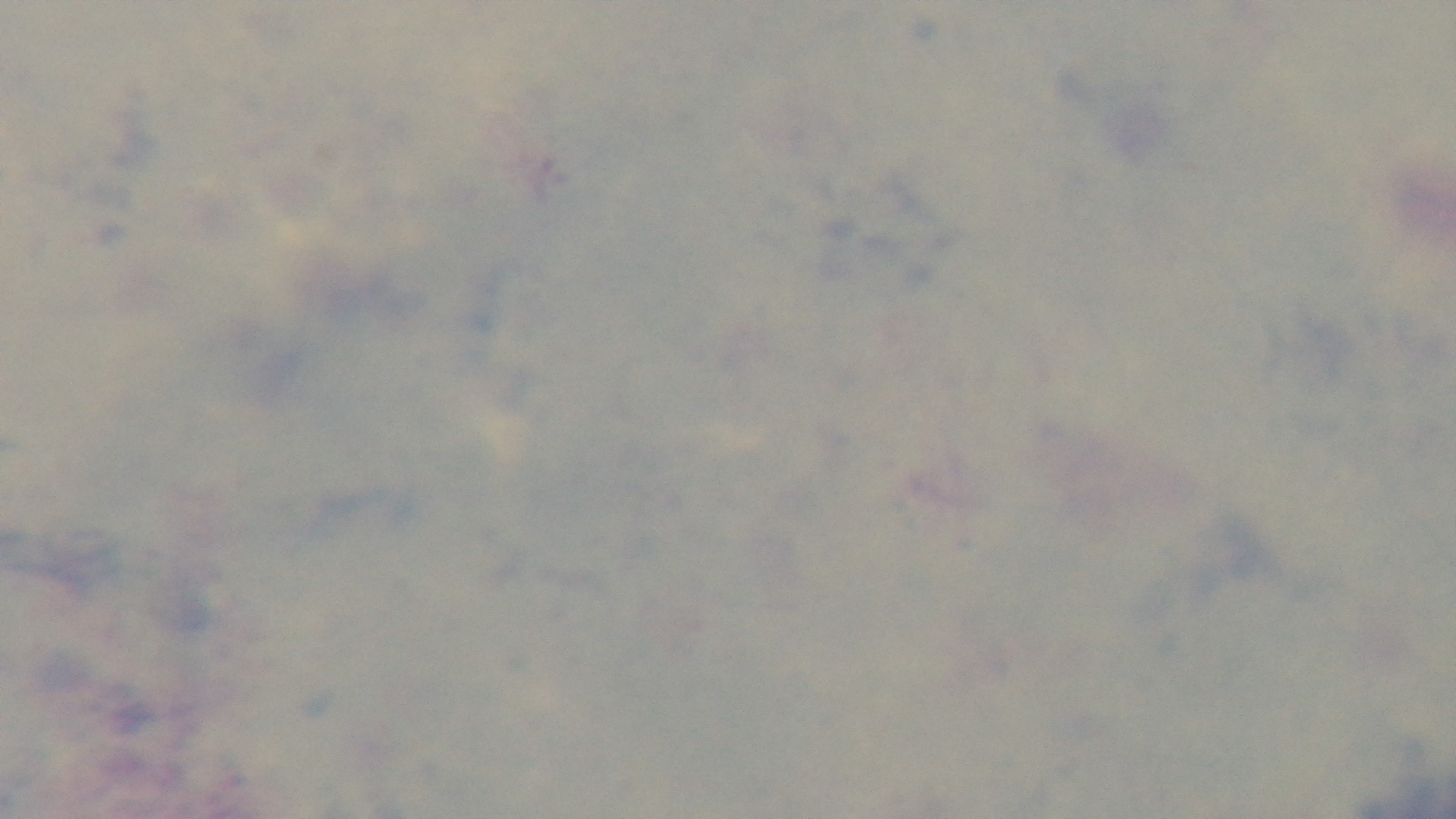

Summary:
  - Objective: 100x oil immersion
  - Field of view: single
  - Modality: light microscopy
  - Malaria status: uninfected
  - Stain: Giemsa
  - Preparation: thick
  - Capture: mounted 4K digital camera